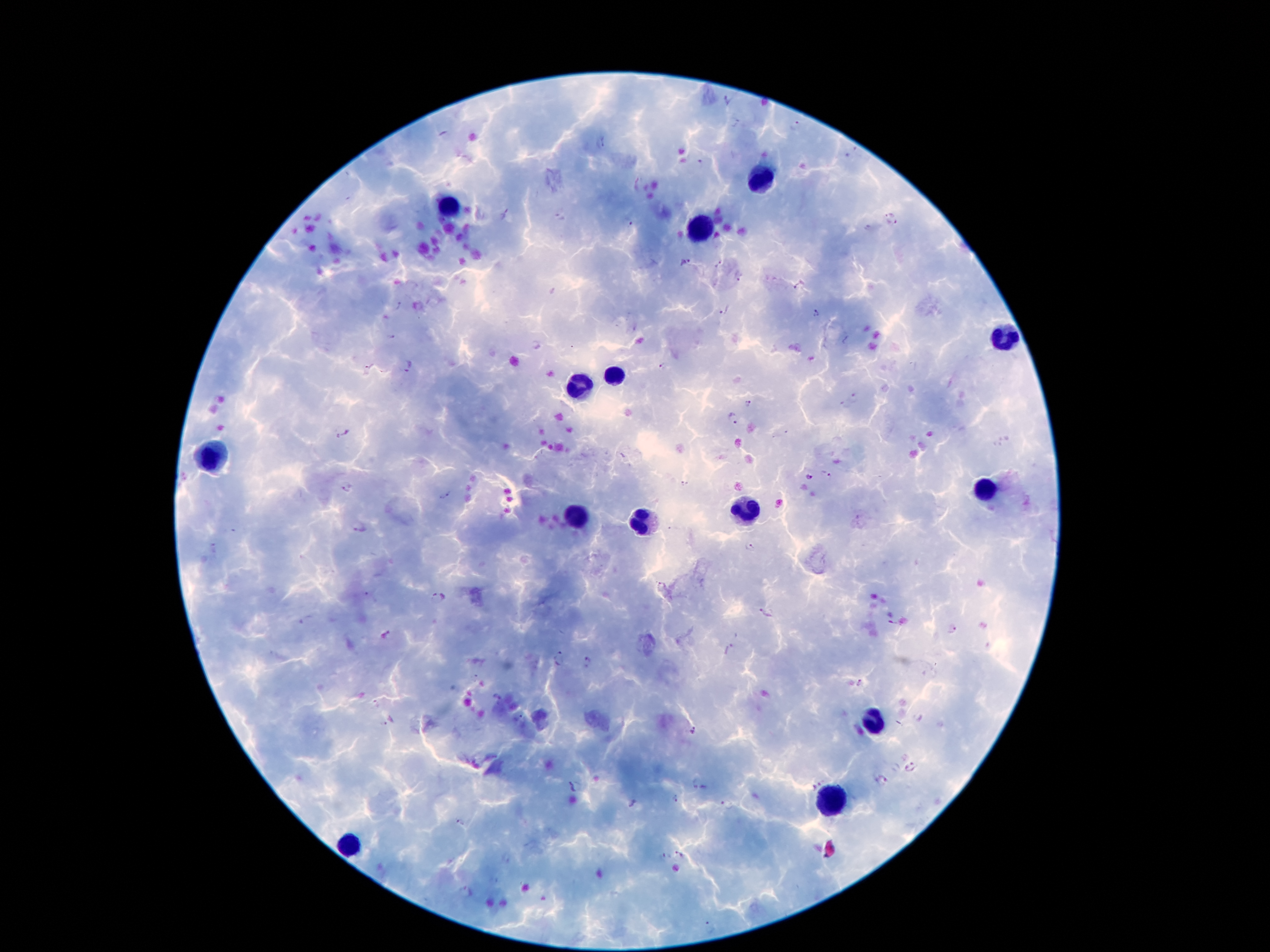 Approximate centers as {x, y} in pixels. Plasmodium parasite locations: {726, 100}, {735, 122}, {795, 125}, {603, 143}, {702, 163}, {889, 211}, {505, 213}, {561, 217}, {628, 223}, {892, 224}, {685, 263}, {719, 263}, {741, 277}, {798, 286}, {398, 306}, {725, 312}, {814, 313}, {390, 337}, {662, 366}, {408, 367}, {366, 371}, {856, 397}, {748, 404}, {844, 406}, {732, 419}, {342, 433}, {826, 474}, {808, 477}, {683, 485}, {347, 489}, {446, 496}, {360, 527}, {749, 548}, {215, 549}, {660, 585}, {438, 598}, {766, 613}, {306, 619}, {892, 622}, {951, 631}, {387, 635}, {734, 646}, {559, 659}, {587, 664}, {860, 684}, {496, 698}, {377, 703}, {520, 718}, {379, 725}, {693, 731}, {911, 767}, {880, 780}, {696, 784}, {813, 784}, {576, 787}, {676, 799}, {727, 804}, {458, 823}, {681, 854}, {661, 857}, {465, 890}, {710, 928}. Leukocyte locations: {763, 177}, {450, 206}, {700, 229}, {1007, 340}, {614, 374}, {580, 387}, {211, 456}, {986, 491}, {746, 509}, {572, 515}, {643, 523}, {874, 721}, {832, 800}, {349, 844}. Thick blood smear. Giemsa stain. 100x magnification. Image is 1270×952 pixels. Patient malaria status: positive for Plasmodium falciparum. One field from this slide. Photographed through the microscope eyepiece with a smartphone camera.